Classify this cell by malaria status.
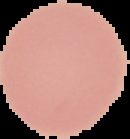
It is uninfected.

Image is 130×139 pixels. From a thin blood smear. Cell region segmented out of the field of view; the surrounding area is masked to black.